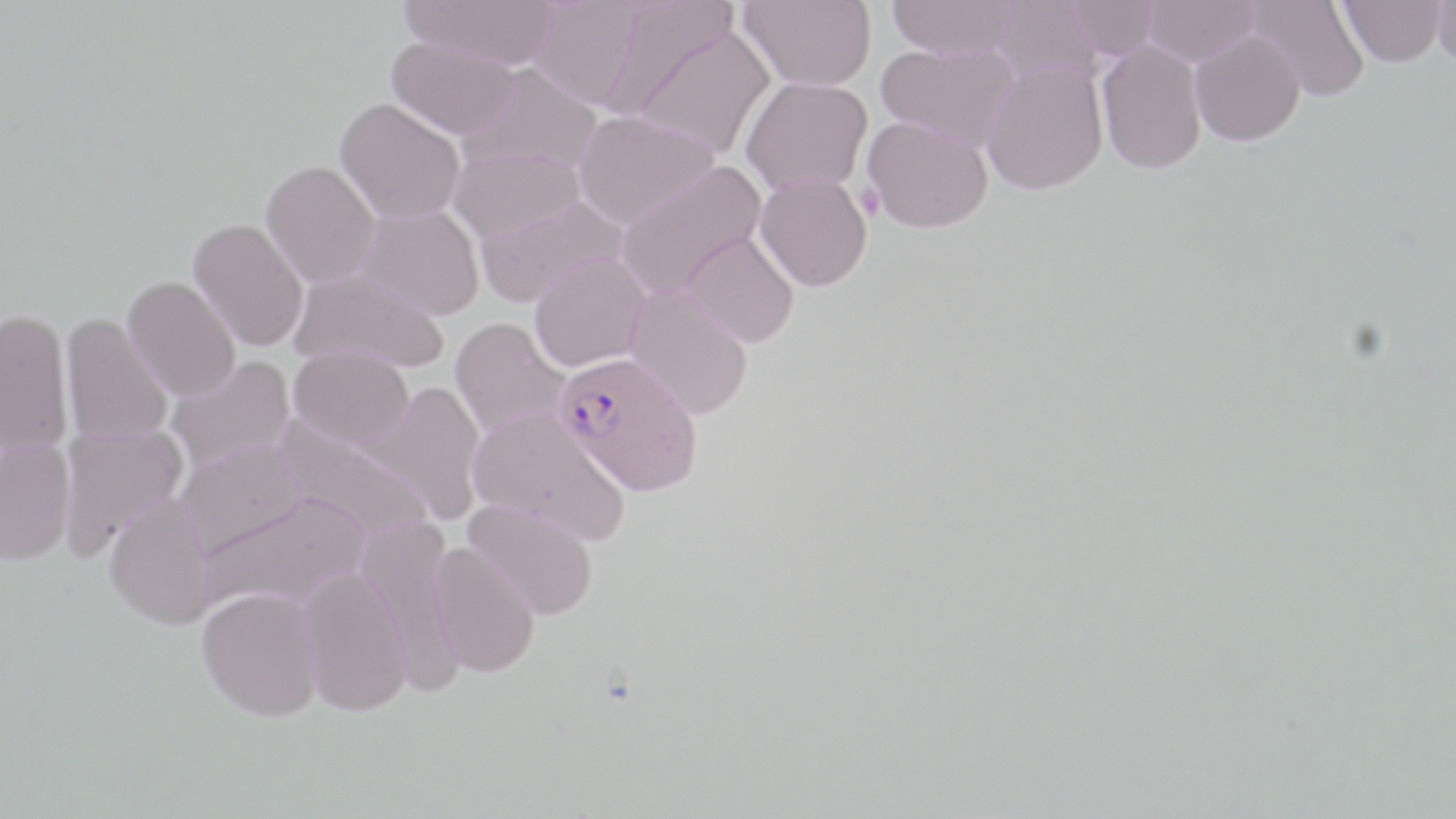
Summary:
  - Coordinate format: approximate bounding boxes as [x1, y1, x2, y2] in pixels
  - Plasmodium falciparum-infected red blood cell locations: [554, 351, 703, 496]
  - Uninfected red blood cell locations: [400, 0, 561, 69], [526, 0, 643, 111], [603, 0, 740, 118], [739, 0, 876, 91], [886, 0, 1021, 59], [1066, 0, 1160, 60], [1141, 0, 1261, 67], [1338, 0, 1447, 67], [1433, 0, 1456, 70], [990, 1, 1101, 88], [1247, 1, 1370, 103], [629, 23, 776, 160], [1190, 30, 1305, 147], [386, 36, 520, 140], [1097, 39, 1209, 175], [875, 41, 1018, 152], [981, 60, 1108, 195], [457, 62, 601, 177], [741, 76, 872, 195], [334, 98, 465, 225], [571, 110, 719, 230], [863, 115, 993, 233], [449, 148, 585, 242], [261, 161, 380, 287], [615, 162, 767, 299], [754, 171, 872, 292], [473, 194, 629, 308], [355, 204, 484, 320], [188, 218, 309, 352], [680, 230, 799, 347], [528, 252, 650, 373], [289, 266, 449, 374], [122, 276, 240, 402], [624, 284, 753, 420], [0, 308, 74, 455], [60, 312, 174, 447], [449, 317, 571, 443], [288, 346, 415, 449], [165, 356, 296, 477], [362, 381, 487, 525], [467, 406, 629, 545], [271, 418, 434, 543], [58, 425, 186, 561], [175, 439, 307, 558], [1, 440, 76, 566], [198, 491, 368, 613], [103, 493, 215, 629], [463, 497, 600, 621], [361, 523, 464, 695], [429, 543, 541, 676], [298, 565, 412, 716], [197, 586, 322, 721]
  - Slide-level diagnosis: Plasmodium falciparum
  - Field of view: one of a larger specimen
  - Modality: optical microscopy
  - Preparation: thin blood smear
  - Stain: May-Grünwald-Giemsa
  - Image size: 1456×819 pixels
  - Magnification: 1000x